Comment on the morphology of the red blood cells.
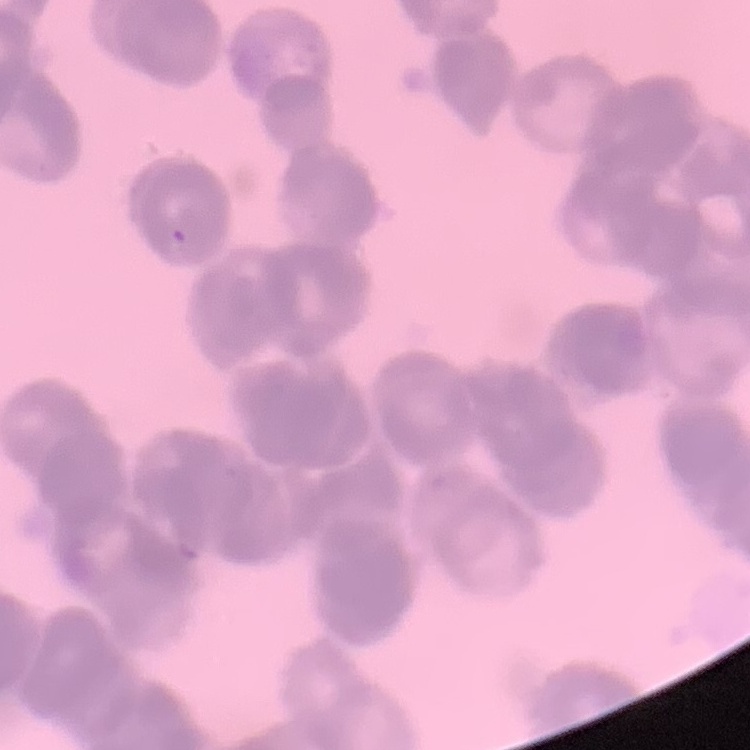
Rouleaux formation.

Stained with either Field's or Giemsa. Thin blood film. Square crop of a larger photomicrograph.